Assess the morphology of the erythrocytes.
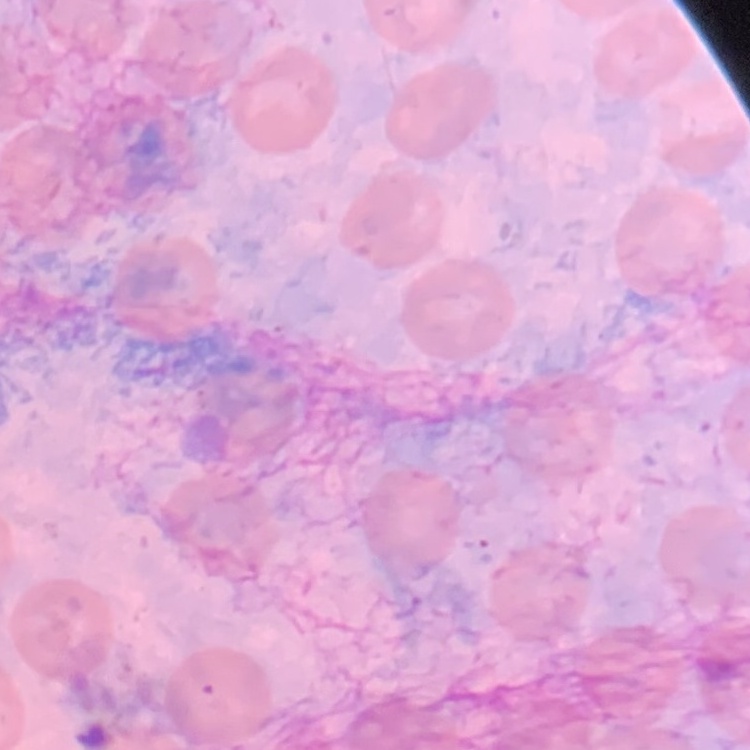

They show no rouleaux formation.

One tile cut from a larger photomicrograph. Thin peripheral smear. Field's or Giemsa stain.